Comment on the morphology of the red blood cells.
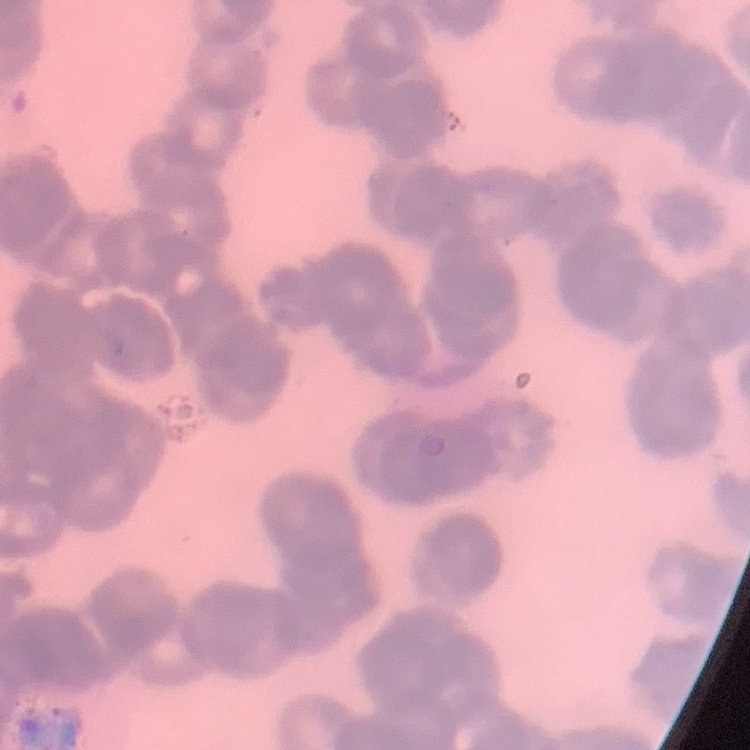
They show rouleaux formation.

{
  "preparation": "thin blood film",
  "image_type": "square crop of a larger photomicrograph",
  "stain": "Field's or Giemsa"
}